Report the malaria status of this cell.
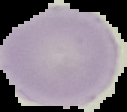
Uninfected.

Summary:
  - Preparation: thin blood smear
  - Image size: 127×112 pixels
  - Image type: segmented cell region with the area outside set to black